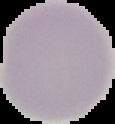 The area outside the segmented cell region is set to black. Malaria status: uninfected. Image is 115×124 pixels. From a thin blood smear.